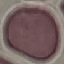

Summary:
  - Malaria status: uninfected
  - Stain: Giemsa
  - Preparation: thin blood film
  - Capture: smartphone camera at the microscope eyepiece
  - Image type: automatically extracted cell patch, resized to 64 × 64 pixels